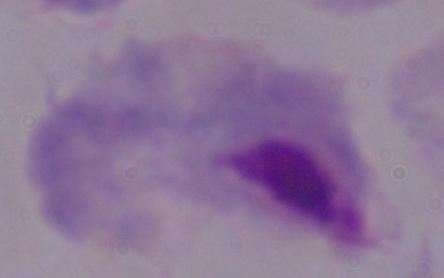
Summary:
  - Identification: trichomonad
  - Modality: micrograph
  - Magnification: 1000x